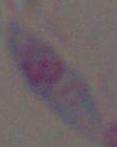
magnification = 1000x
modality = photomicrograph
identification = Toxoplasma gondii